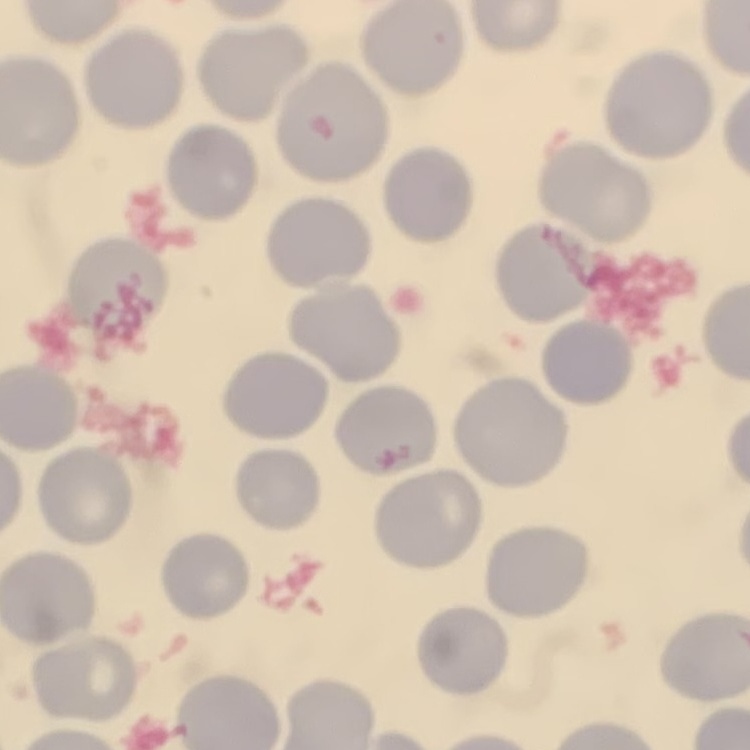

{
  "red_blood_cell_morphology": "no rouleaux formation",
  "stain": "Field's or Giemsa",
  "image_type": "square crop of a larger photomicrograph",
  "preparation": "thin blood film"
}